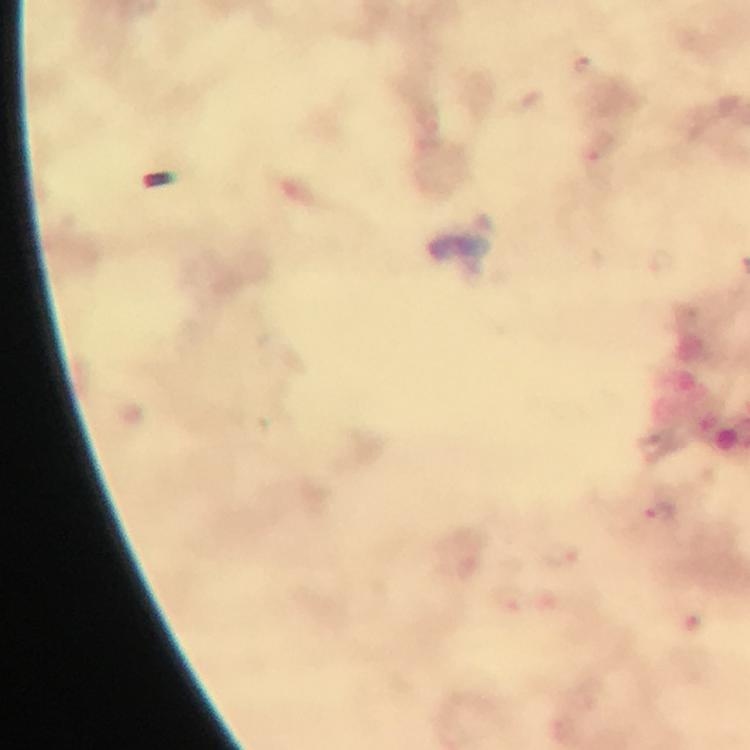

Approximate centers as [x, y] in pixels.
Summary:
  - Malaria parasite locations: [585, 66], [661, 513]
  - Context: from a malaria diagnostic workup
  - Magnification: 100x
  - Cropped from: one field of view
  - Capture: smartphone camera through the microscope
  - Preparation: thick blood film
  - Image size: 750×750 pixels
  - Stain: Giemsa
  - Immersion oil: applied